Report the malaria status of this cell.
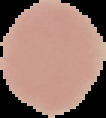
Uninfected.

Segmented cell region on a black background. Image is 106×118 pixels. From a thin blood film.